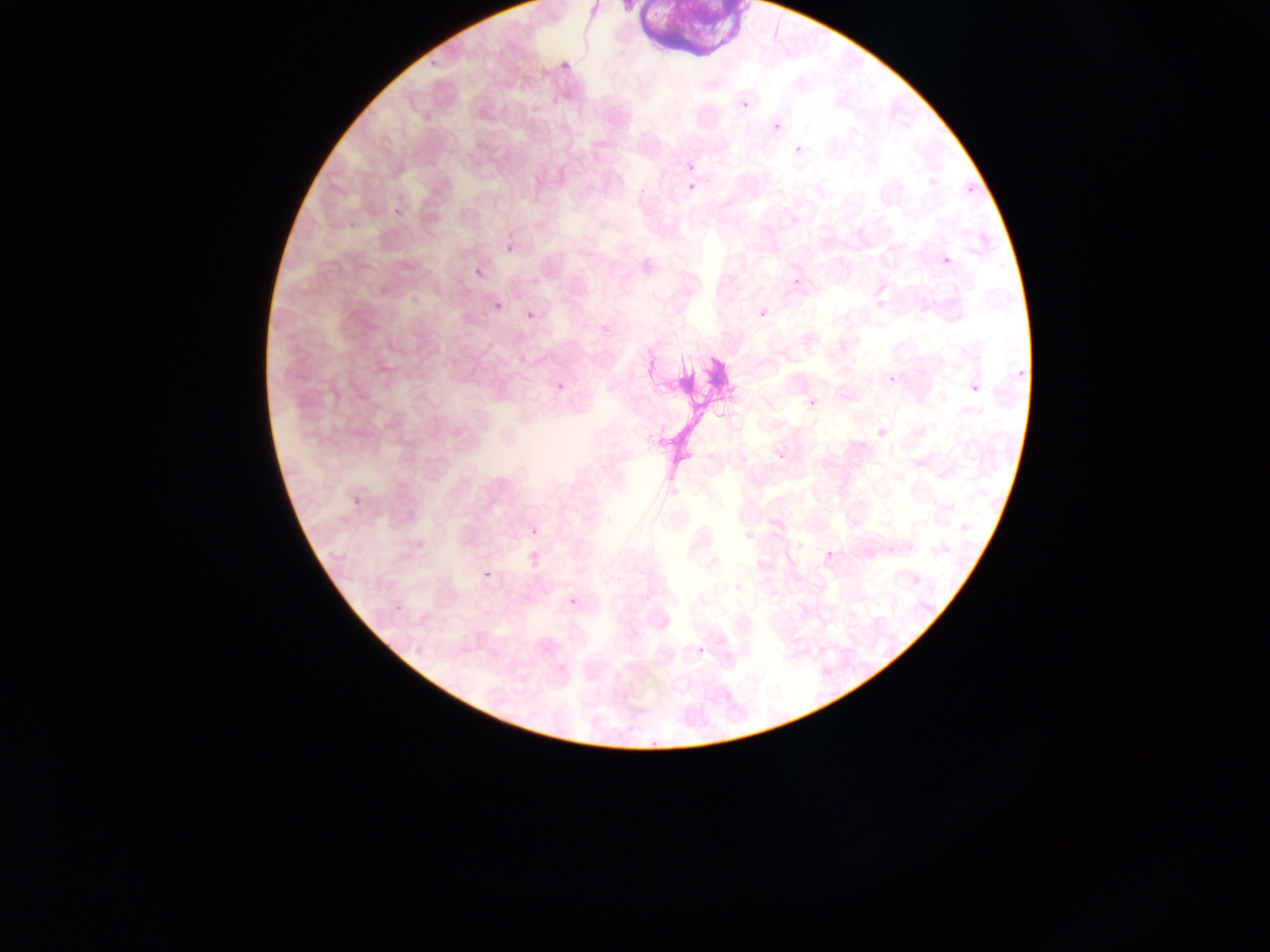
Approximate bounding boxes as {left, top, right, bottom} in pixels. Plasmodium parasite locations: {563, 58, 578, 70}, {740, 98, 752, 107}, {772, 114, 788, 128}, {791, 144, 804, 154}, {687, 183, 695, 191}, {969, 186, 979, 200}, {394, 206, 410, 216}, {506, 242, 520, 253}, {940, 256, 953, 267}, {474, 265, 484, 275}, {791, 274, 805, 287}, {493, 300, 506, 312}, {525, 309, 537, 321}, {756, 309, 768, 320}, {1009, 364, 1030, 377}, {888, 376, 897, 384}, {965, 376, 987, 398}, {558, 381, 565, 392}, {807, 400, 817, 408}, {779, 454, 785, 462}, {349, 496, 363, 510}, {530, 525, 544, 535}, {825, 550, 835, 559}, {484, 565, 496, 584}, {913, 577, 920, 585}, {391, 591, 412, 612}, {570, 597, 579, 605}, {696, 646, 709, 656}, {651, 736, 659, 746}. Artifact (stain precipitate or debris) locations: {634, 0, 742, 49}, {661, 339, 728, 481}. Mobile-phone photograph taken through the microscope. Single field of view. Thin blood film. Image is 1270×952 pixels. Sample from Ghana.